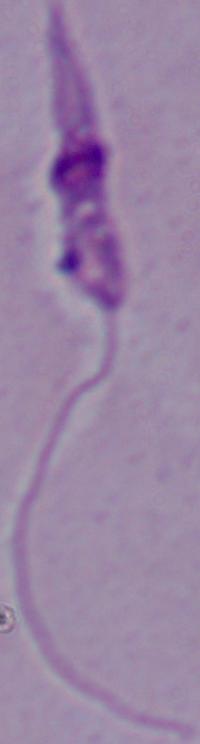 A Leishmania parasite is seen. Micrograph. 1000x magnification.